Report the malaria status of this cell.
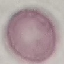
Uninfected.

image_type: cell patch, automatically extracted from a larger field of view and resized to 64 × 64 pixels
preparation: thin smear
stain: Giemsa
capture: smartphone through the microscope eyepiece